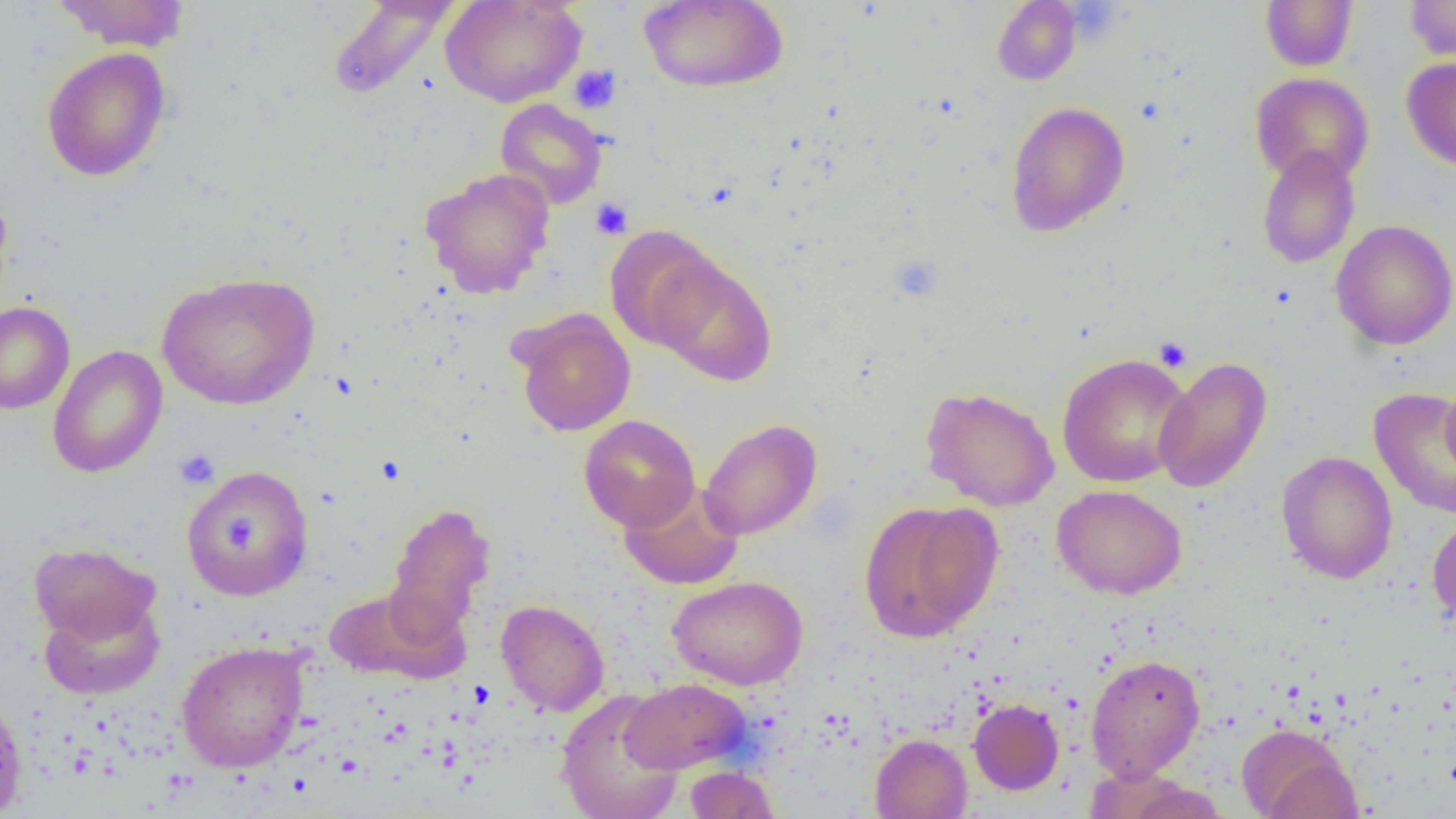

Summary:
  - Coordinate format: approximate bounding boxes as (x1, y1, x2, y2) in pixels
  - Platelet locations: (568, 64, 622, 115), (590, 198, 633, 240), (1153, 336, 1192, 371), (174, 448, 219, 489)
  - Uninfected red blood cell locations: (52, 0, 191, 51), (325, 0, 461, 102), (440, 0, 586, 108), (1404, 0, 1456, 61), (638, 1, 788, 93), (992, 1, 1081, 85), (1259, 1, 1358, 71), (41, 47, 171, 182), (1401, 57, 1456, 172), (1249, 73, 1374, 186), (494, 99, 608, 209), (1004, 101, 1130, 237), (1257, 145, 1361, 269), (420, 167, 556, 299), (0, 186, 16, 313), (1330, 219, 1456, 350), (603, 225, 725, 351), (651, 256, 778, 386), (156, 271, 320, 410), (0, 302, 75, 414), (513, 310, 635, 437), (48, 346, 167, 478), (1057, 352, 1194, 488), (1153, 356, 1272, 494), (1441, 380, 1456, 482), (920, 386, 1060, 511), (1369, 387, 1456, 520), (578, 414, 701, 532), (699, 418, 822, 540), (1277, 450, 1397, 584), (181, 464, 314, 602), (619, 481, 744, 591), (1052, 484, 1187, 600), (859, 501, 1002, 642), (385, 502, 497, 639), (1427, 514, 1456, 629), (28, 541, 161, 646), (668, 575, 808, 690), (322, 584, 468, 684), (39, 595, 165, 700), (496, 599, 609, 716), (176, 641, 309, 772), (1086, 653, 1205, 781), (621, 678, 750, 774), (555, 689, 684, 819), (0, 691, 28, 819), (969, 698, 1064, 795), (1235, 723, 1359, 819), (870, 733, 972, 818), (684, 766, 780, 818), (1122, 777, 1231, 819)
  - Slide-level diagnosis: negative for blood parasites
  - Image size: 1456×819 pixels
  - Field of view: single
  - Preparation: thin blood smear
  - Magnification: 1000x
  - Modality: optical microscopy